Give the position of every Plasmodium parasite.
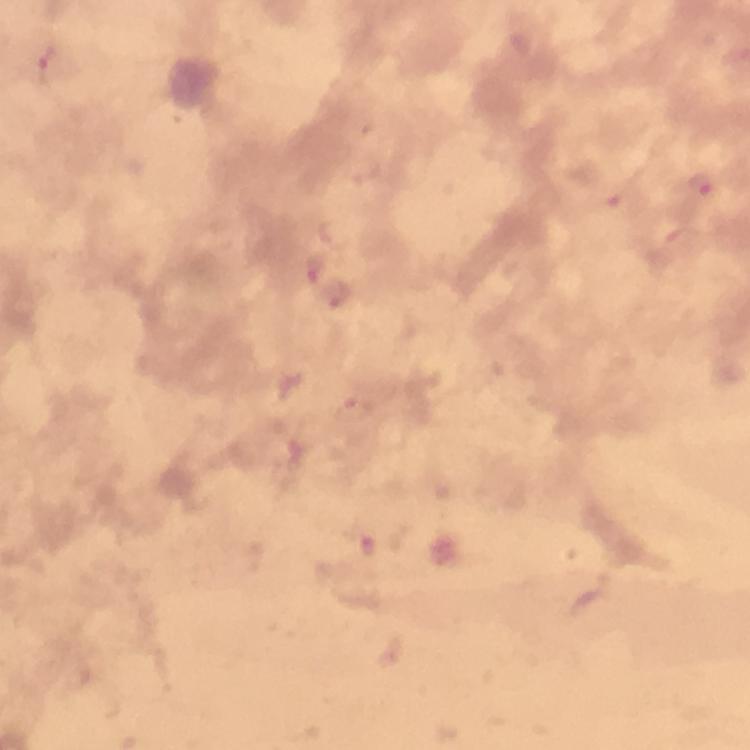

Approximate centers as [x, y] in pixels.
Plasmodium parasites: [55, 64], [700, 184], [612, 197], [314, 268], [356, 409], [364, 545].

At 100x magnification. Smartphone photograph taken through a microscope. Image is 750×750 pixels. Immersion oil was used. From a malaria diagnostic workup. Thick blood film. Cropped region of a single field of view. Giemsa stain.